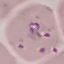
Result: malaria parasites detected. Giemsa-stained preparation. Automatically extracted cell patch, resized to 64 × 64 pixels. Acquired by smartphone through the microscope eyepiece. Thin smear of blood.